Comment on the morphology of the red blood cells.
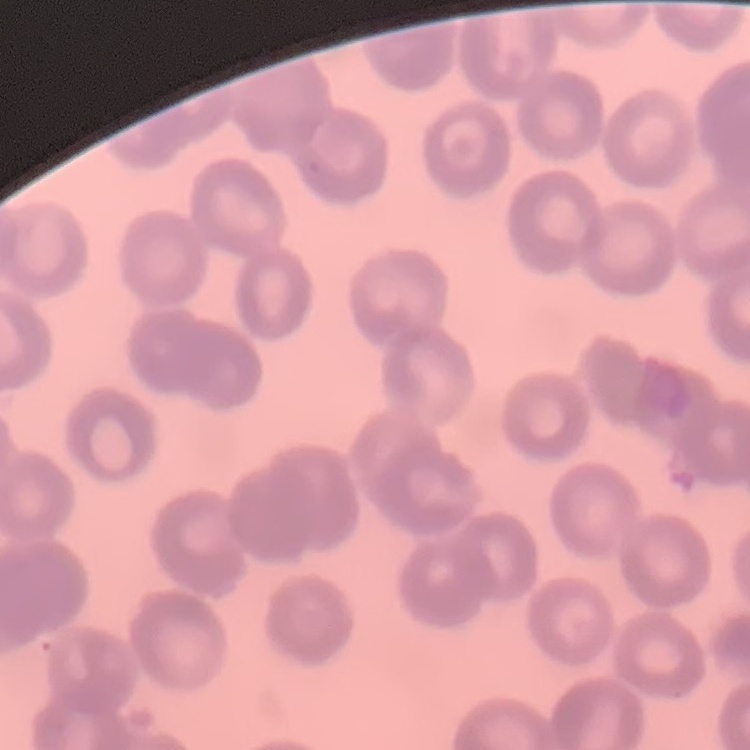
No rouleaux formation.

Thin blood film. One tile cut from a larger photomicrograph. Field's or Giemsa stain.